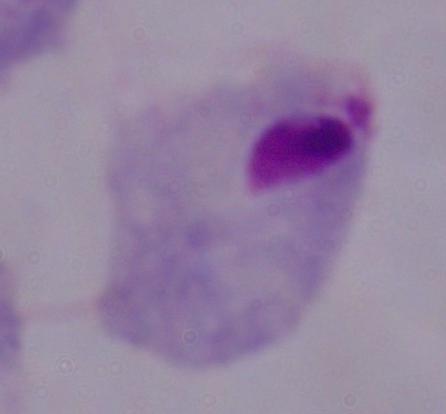
{
  "modality": "micrograph",
  "identification": "trichomonad",
  "magnification": "1000x"
}